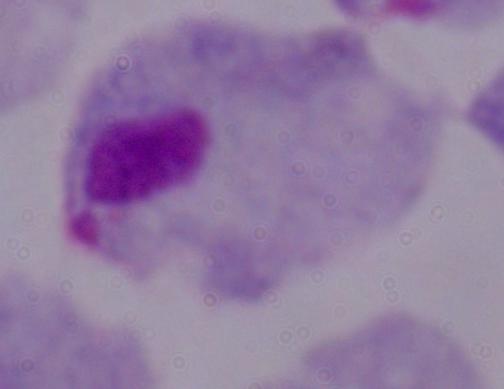

identification: trichomonad
magnification: 1000x
modality: micrograph